Evaluate for Plasmodium parasites.
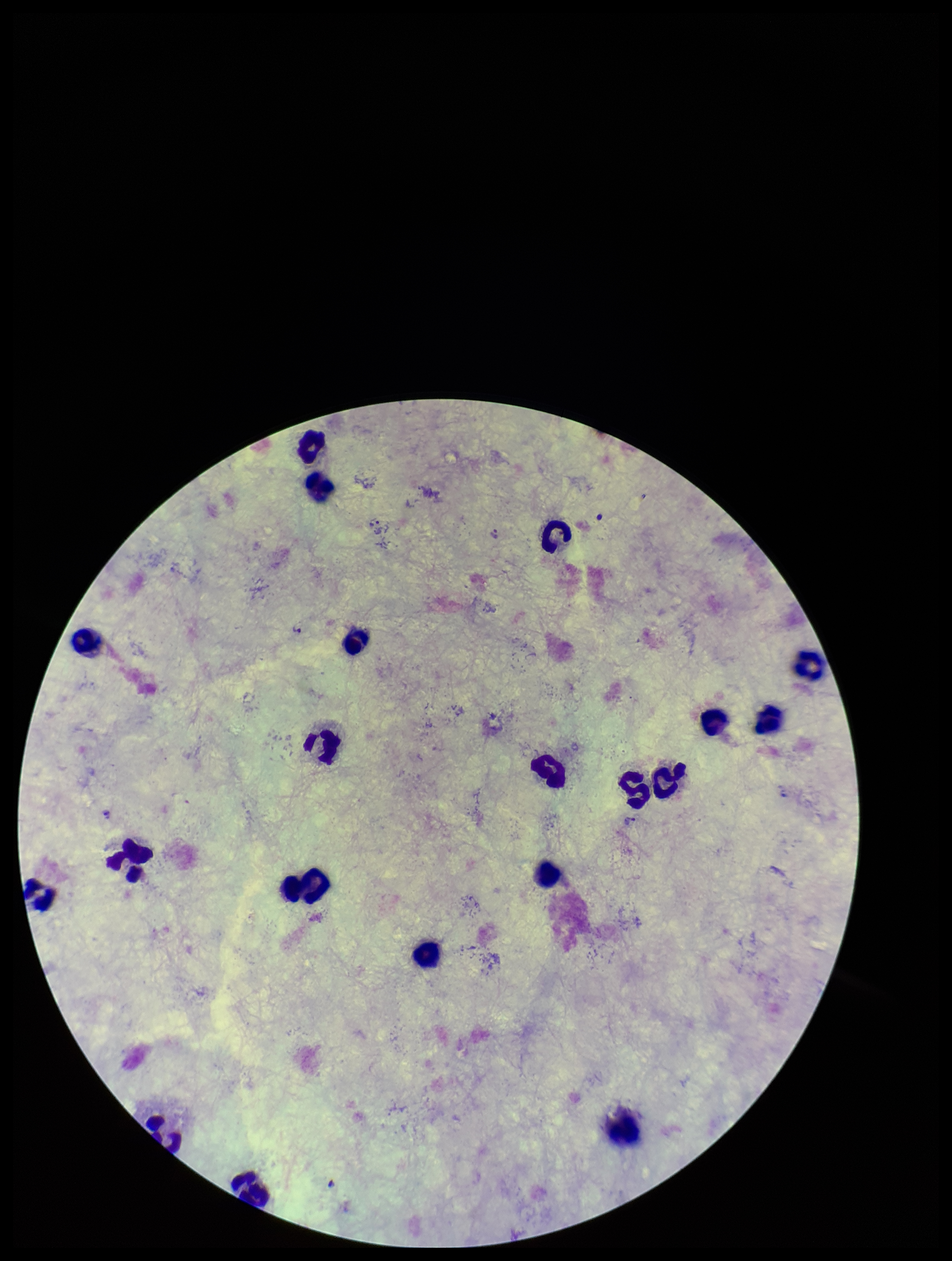
Detected.

leukocyte count = 20
stain = Giemsa
image size = 952×1261 pixels
field of view = single
capture = smartphone photograph through the microscope eyepiece
patient malaria status = positive
parasite count = 4
species reported for this patient = Plasmodium vivax
preparation = thick smear